Report the malaria status of this cell.
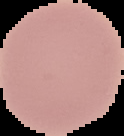

It is uninfected.

Summary:
  - Preparation: thin blood smear
  - Image size: 124×136 pixels
  - Image type: segmented cell region with the area outside set to black